State which parasite is depicted.
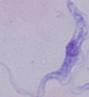

A trypanosome.

Summary:
  - Magnification: 1000x
  - Modality: micrograph